Identify the preparation type.
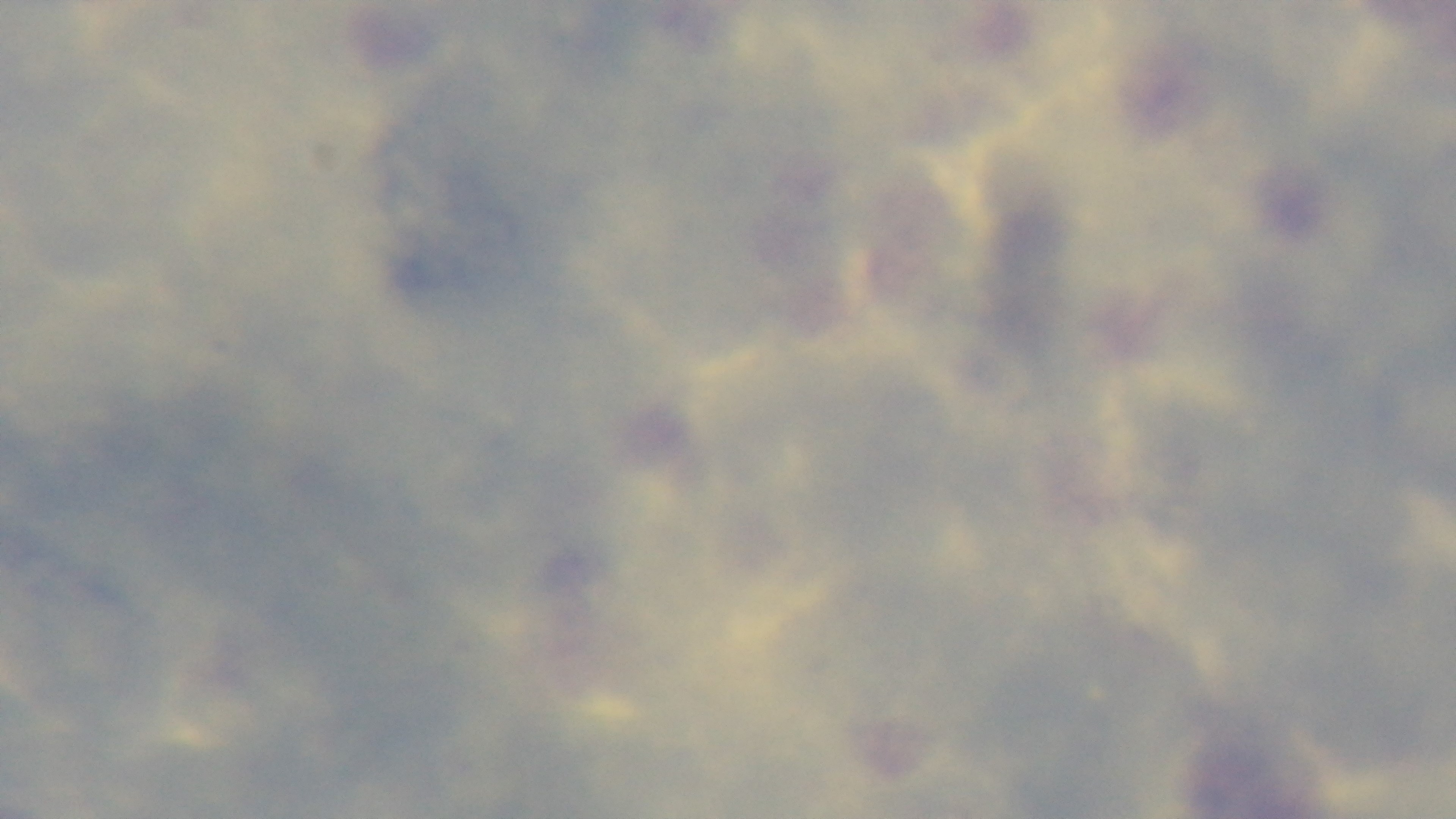
A thick smear.

Single field of view. Captured with a mounted 4K digital camera. Photomicrograph. Oil-immersion objective, 100x. Giemsa-stained. Malaria status: negative.